State which parasite is depicted.
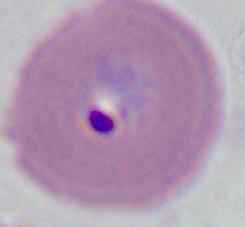
Plasmodium.

Summary:
  - Magnification: 400x or 1000x
  - Modality: micrograph